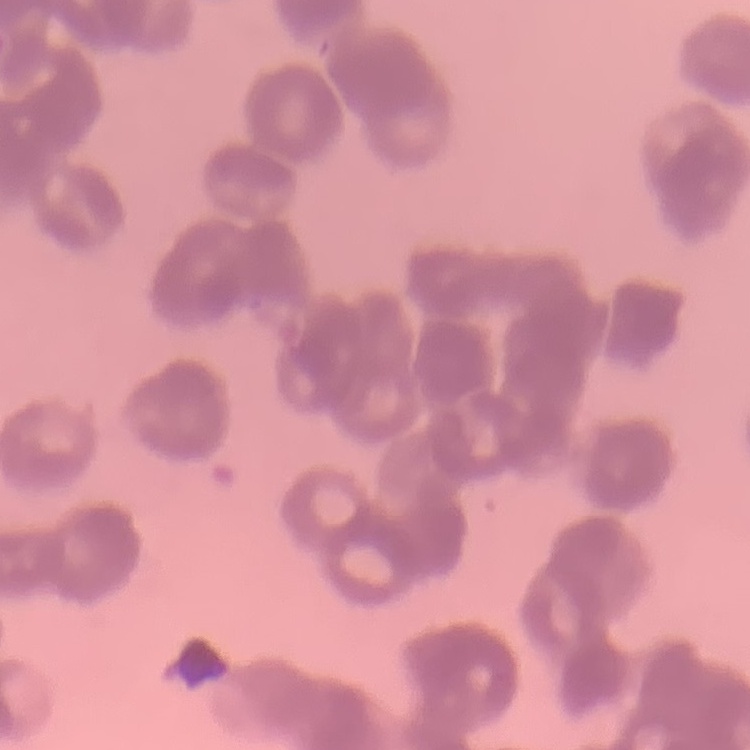

erythrocyte morphology = rouleaux formation
stain = Field's or Giemsa
preparation = thin peripheral smear
image type = one tile cut from a larger photomicrograph